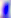
Summary:
  - Modality: micrograph
  - Identification: Toxoplasma gondii
  - Magnification: 400x